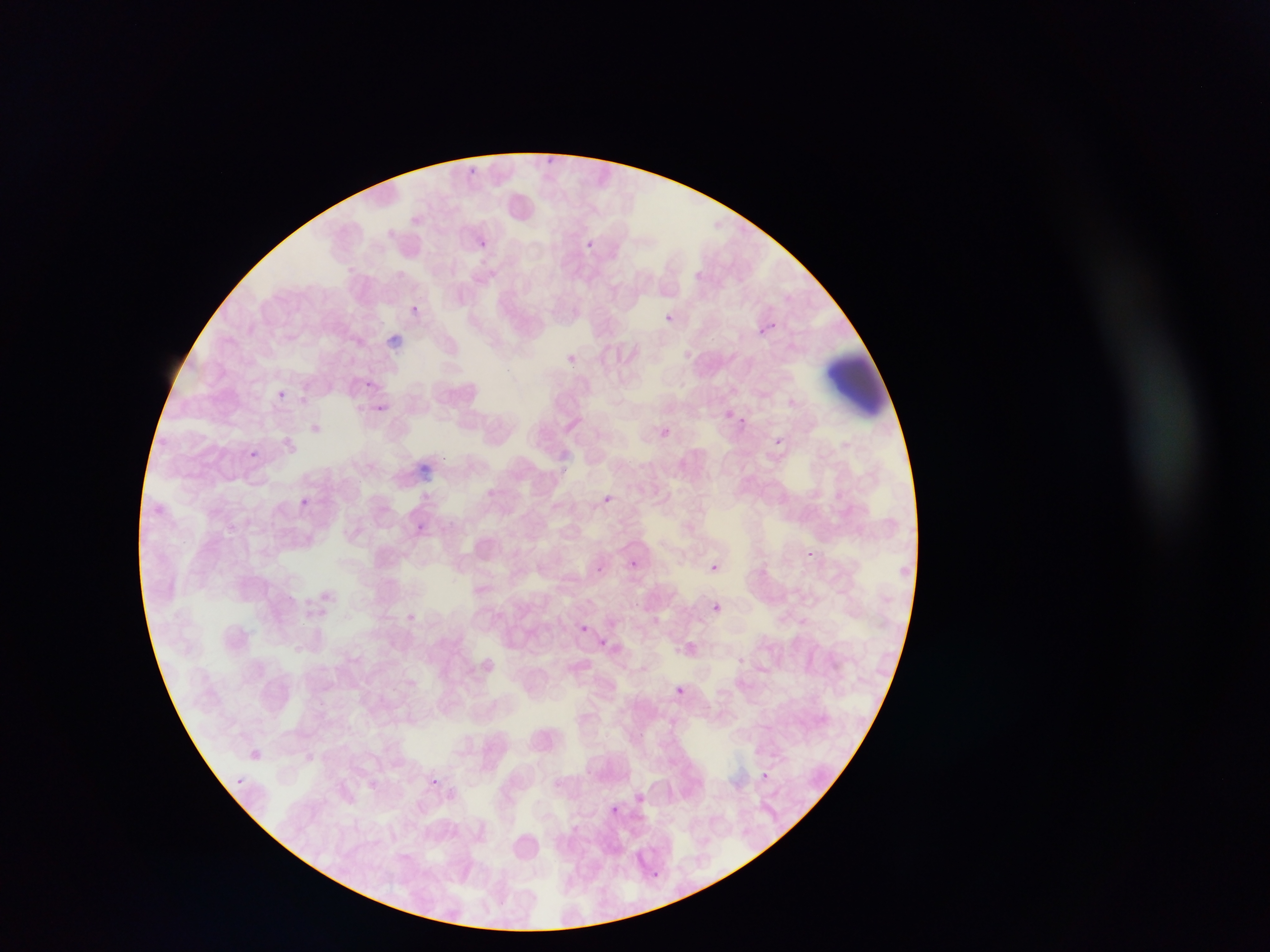
preparation: thin blood film
field_of_view: single
image_size: 1270×952 pixels
capture: mobile-phone photograph through a microscope
artifact_stain_precipitate_or_debris_locations: 'approximate bounding boxes as {left, top, right, bottom} in pixels: {387, 330, 407, 348}, {822, 354, 892, 419}, {421, 460, 437, 483}'
country: Ghana
plasmodium_parasite_locations: 'approximate bounding boxes as {left, top, right, bottom} in pixels: {546, 155, 560, 163}, {467, 166, 484, 176}, {480, 242, 485, 250}, {588, 242, 598, 256}, {409, 303, 422, 312}, {664, 315, 671, 323}, {754, 320, 776, 340}, {565, 356, 580, 367}, {361, 379, 373, 388}, {272, 387, 293, 408}, {378, 404, 386, 411}, {729, 412, 747, 428}, {737, 415, 748, 426}, {654, 424, 672, 441}, {773, 437, 783, 447}, {247, 449, 260, 461}, {558, 462, 575, 482}, {600, 493, 616, 506}, {299, 497, 311, 507}, {416, 522, 428, 534}, {807, 548, 824, 563}, {626, 558, 639, 570}, {706, 562, 720, 574}, {714, 602, 733, 616}, {574, 619, 594, 638}, {591, 634, 613, 654}, {673, 686, 686, 699}, {675, 686, 684, 694}, {241, 744, 268, 767}, {758, 769, 772, 781}, {232, 774, 248, 790}, {432, 775, 446, 789}, {607, 800, 622, 813}, {649, 868, 660, 880}'